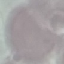

Malaria status: uninfected. Giemsa-stained preparation. Photographed with a smartphone camera at the microscope eyepiece. Thin smear of blood. Automatically extracted cell patch, resized to 64 × 64 pixels.